Classify this cell by malaria status.
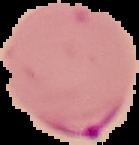
It is parasitized.

Cell region segmented out of the field of view; the surrounding area is masked to black. Image is 139×145 pixels. From a thin blood smear.